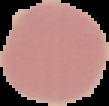 Malaria status: uninfected. From a thin blood smear. Image is 109×106 pixels. The area outside the segmented cell region is set to black.